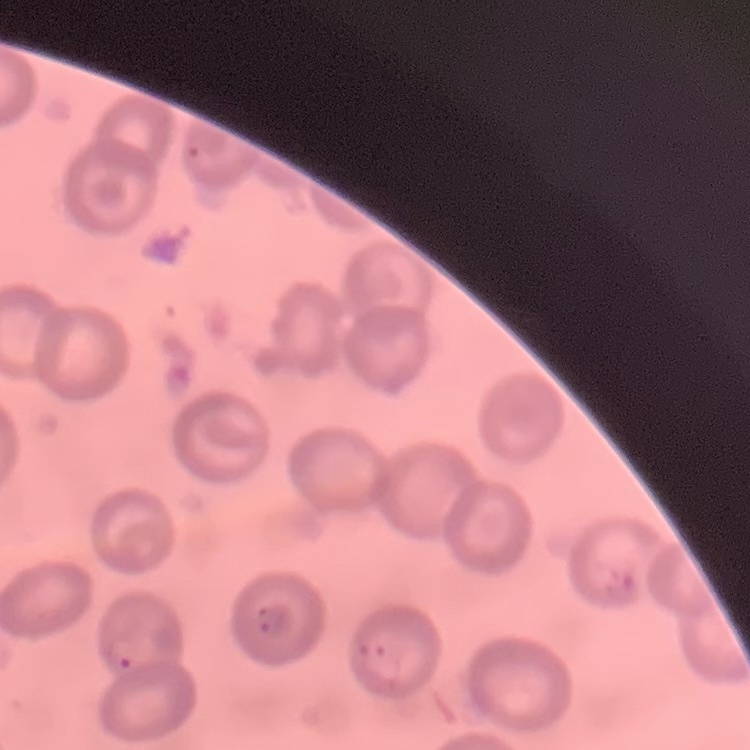

Summary:
  - Erythrocyte morphology: no rouleaux formation
  - Stain: Field's or Giemsa
  - Preparation: thin blood smear
  - Image type: one tile cut from a larger photomicrograph